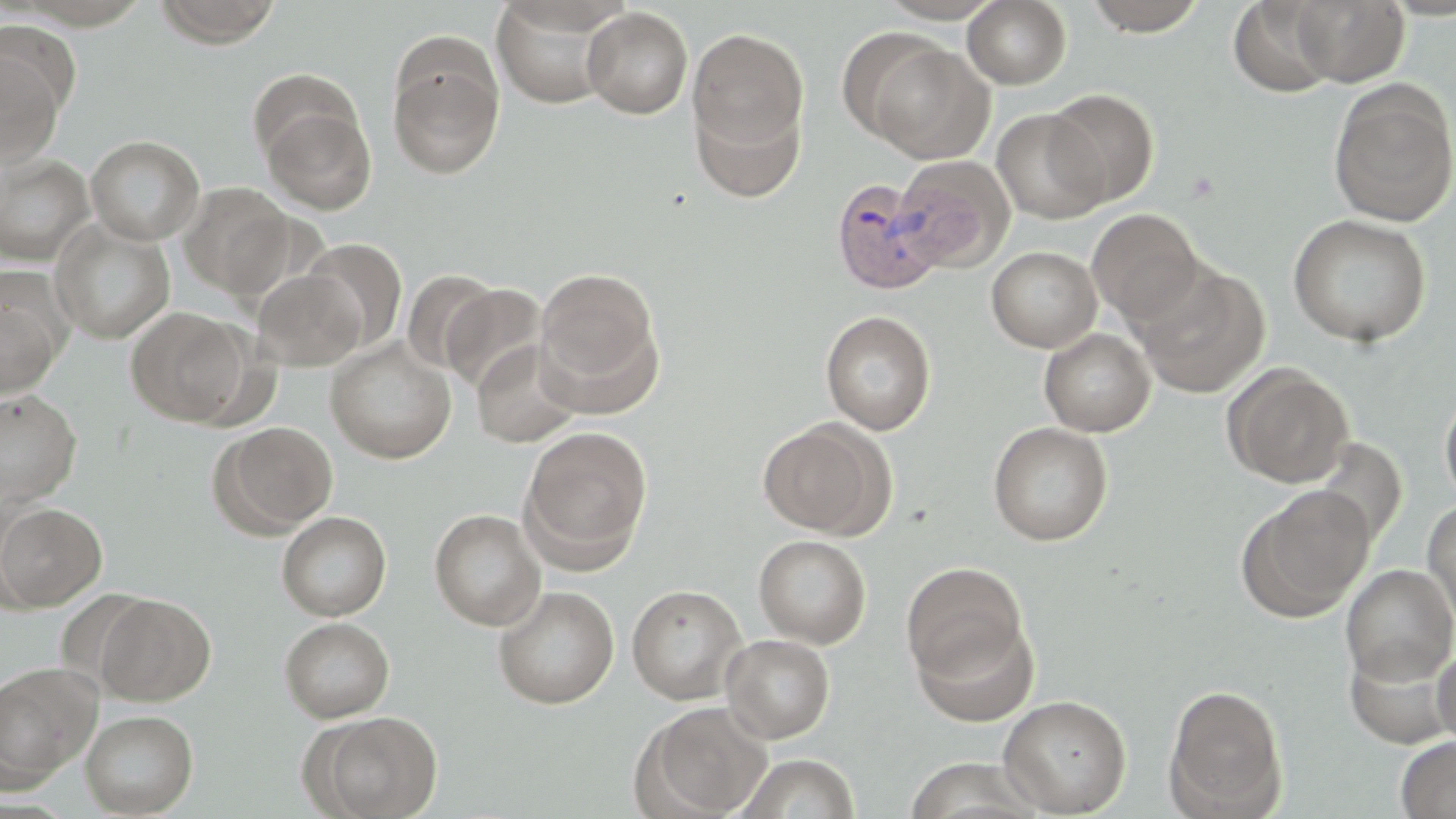
Approximate bounding boxes as (x1, y1, x2, y2) in pixels. Plasmodium vivax-infected red blood cell locations: (830, 178, 947, 295). Uninfected red blood cell locations: (153, 0, 282, 47), (875, 0, 1006, 23), (963, 0, 1071, 89), (1082, 0, 1210, 36), (1289, 0, 1410, 86), (490, 1, 620, 110), (1229, 1, 1337, 98), (582, 7, 693, 119), (688, 27, 809, 158), (861, 37, 996, 164), (0, 45, 67, 168), (387, 48, 505, 180), (1328, 80, 1456, 228), (1045, 89, 1159, 207), (691, 90, 807, 206), (260, 101, 376, 215), (992, 108, 1109, 224), (86, 134, 205, 245), (0, 153, 95, 266), (892, 157, 1014, 273), (178, 182, 296, 299), (1087, 208, 1203, 325), (1288, 214, 1432, 347), (50, 219, 174, 344), (300, 238, 407, 351), (986, 246, 1102, 353), (1134, 263, 1269, 399), (534, 267, 662, 398), (252, 269, 365, 370), (401, 270, 501, 376), (0, 282, 66, 401), (441, 283, 548, 393), (125, 306, 251, 426), (820, 310, 936, 435), (1039, 328, 1156, 437), (325, 338, 457, 463), (469, 339, 584, 449), (1223, 363, 1355, 488), (1439, 389, 1456, 510), (0, 390, 83, 507), (757, 419, 890, 538), (217, 421, 338, 534), (988, 421, 1112, 545), (519, 426, 653, 565), (1312, 437, 1406, 549), (1237, 485, 1375, 621), (1422, 498, 1456, 631), (0, 502, 107, 613), (428, 508, 546, 631), (277, 511, 391, 621), (754, 535, 871, 648), (901, 562, 1029, 682), (1340, 564, 1456, 685), (627, 584, 747, 704), (493, 585, 619, 709), (55, 588, 157, 695), (96, 594, 214, 705), (912, 614, 1039, 727), (279, 617, 394, 722), (722, 634, 835, 742), (1344, 639, 1456, 749), (1433, 645, 1456, 750), (0, 664, 98, 789), (1164, 683, 1288, 819), (998, 694, 1132, 816), (635, 701, 771, 818), (80, 709, 198, 817), (313, 711, 443, 819), (1396, 737, 1456, 818), (736, 752, 860, 818), (904, 758, 1046, 818). Slide-level diagnosis: Plasmodium vivax. Optical microscopy. One field of a larger specimen. 1000x magnification. May-Grünwald-Giemsa-stained preparation. Thin blood smear. Image is 1456×819 pixels.